Outline each blood parasite and name the species.
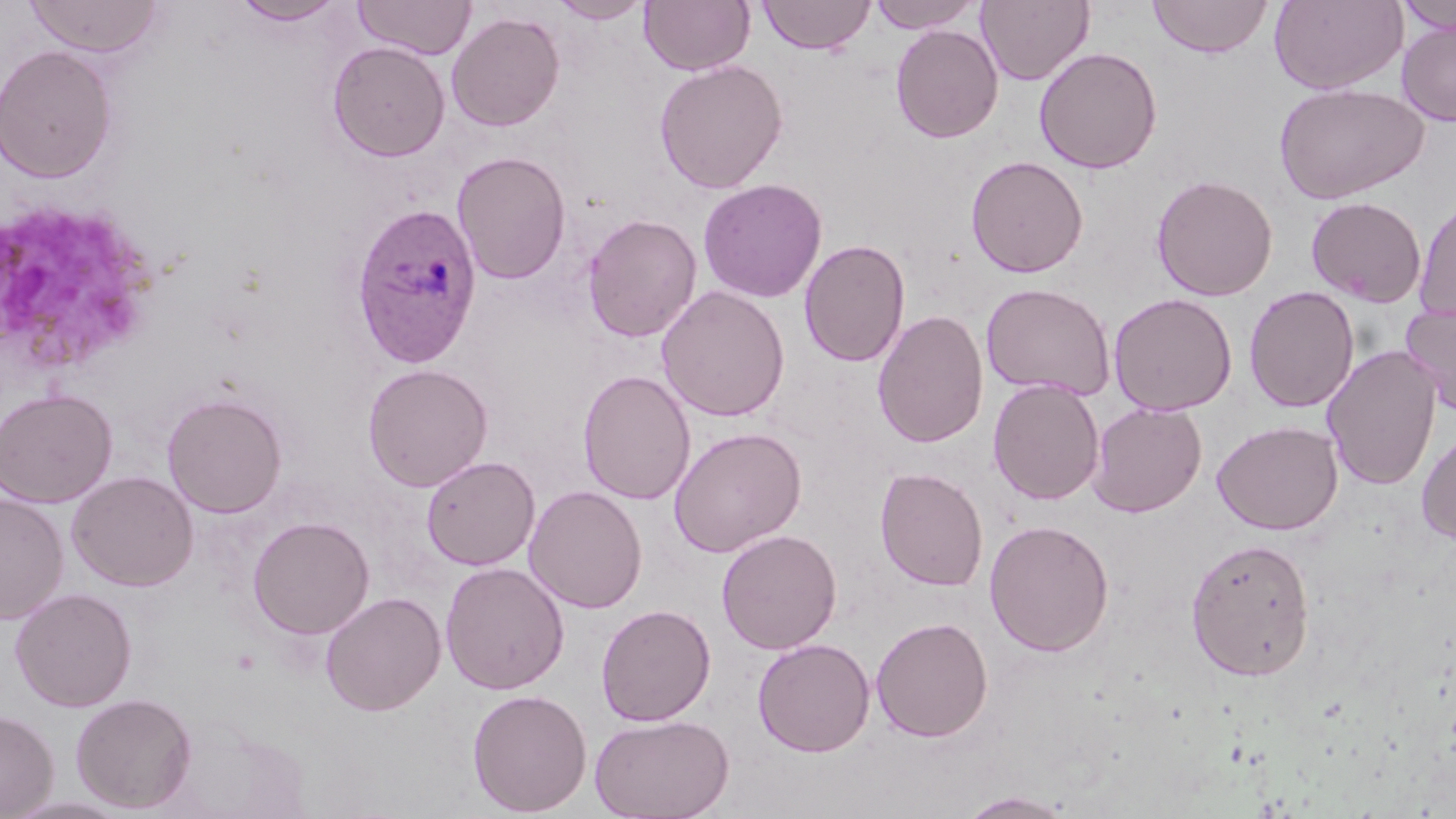
Approximate bounding boxes as [x1, y1, x2, y2] in pixels.
Plasmodium ovale-infected red blood cells: [351, 203, 481, 368].
No Plasmodium falciparum, Plasmodium malariae, Plasmodium vivax, Babesia divergens, or Trypanosoma brucei observed.

Platelet locations: [0, 202, 164, 374]. Uninfected red blood cell locations: [24, 0, 162, 58], [231, 0, 346, 26], [354, 0, 476, 59], [549, 0, 652, 23], [640, 0, 755, 76], [758, 0, 875, 55], [867, 0, 984, 33], [975, 0, 1094, 85], [1147, 0, 1273, 58], [1269, 0, 1408, 95], [1395, 0, 1456, 36], [446, 12, 565, 131], [1396, 22, 1456, 126], [890, 24, 1004, 143], [327, 41, 451, 162], [0, 44, 118, 183], [1034, 46, 1162, 174], [654, 59, 789, 194], [1273, 81, 1429, 204], [452, 151, 572, 285], [966, 155, 1089, 278], [1151, 174, 1278, 301], [697, 178, 828, 303], [1305, 196, 1427, 307], [1414, 196, 1456, 325], [582, 214, 702, 343], [799, 238, 911, 367], [980, 282, 1116, 400], [656, 285, 791, 422], [1244, 285, 1360, 413], [1108, 293, 1237, 416], [1401, 299, 1456, 416], [872, 309, 989, 449], [1322, 344, 1442, 491], [362, 362, 493, 492], [578, 369, 696, 505], [988, 378, 1105, 505], [0, 388, 118, 508], [162, 392, 288, 519], [1087, 400, 1207, 517], [1211, 419, 1343, 535], [1415, 425, 1456, 544], [669, 427, 807, 557], [422, 455, 540, 570], [875, 467, 989, 592], [67, 470, 198, 591], [524, 485, 647, 613], [0, 495, 69, 624], [247, 516, 375, 639], [984, 519, 1114, 657], [716, 529, 842, 654], [1185, 537, 1316, 681], [440, 562, 569, 695], [10, 587, 137, 712], [320, 591, 446, 716], [596, 604, 715, 725], [870, 616, 993, 742], [752, 638, 875, 757], [467, 688, 592, 816], [70, 692, 197, 813], [0, 709, 59, 818], [589, 713, 735, 819], [957, 791, 1076, 818]. Slide-level diagnosis: Plasmodium ovale. May-Grünwald-Giemsa stain. Light microscopy. Thin blood film. Captured at 1000x magnification. Image is 1456×819 pixels. Single field of view.